Assess the morphology of the red blood cells.
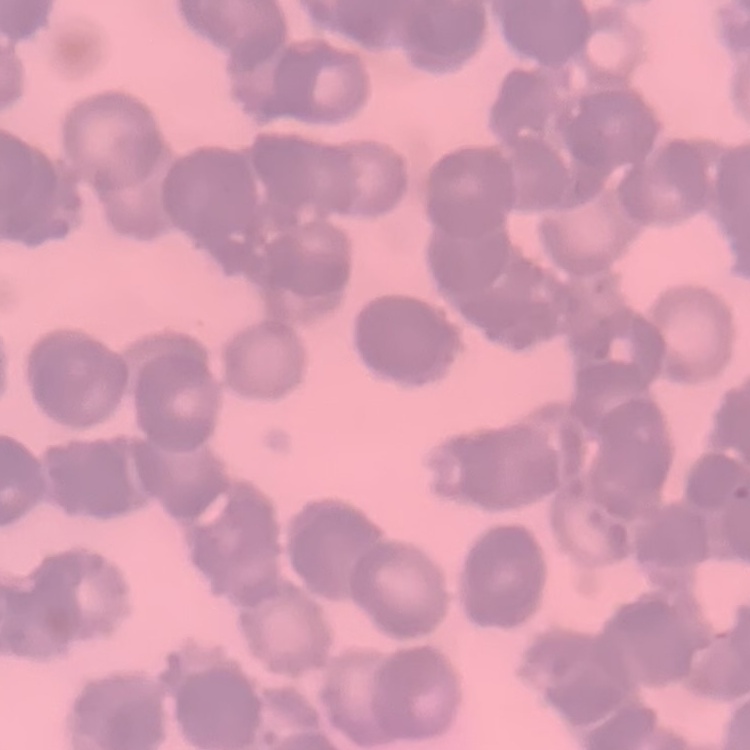
Rouleaux formation.

Thin blood smear. One tile cut from a larger photomicrograph. Stained with either Field's or Giemsa.